Locate every malaria parasite.
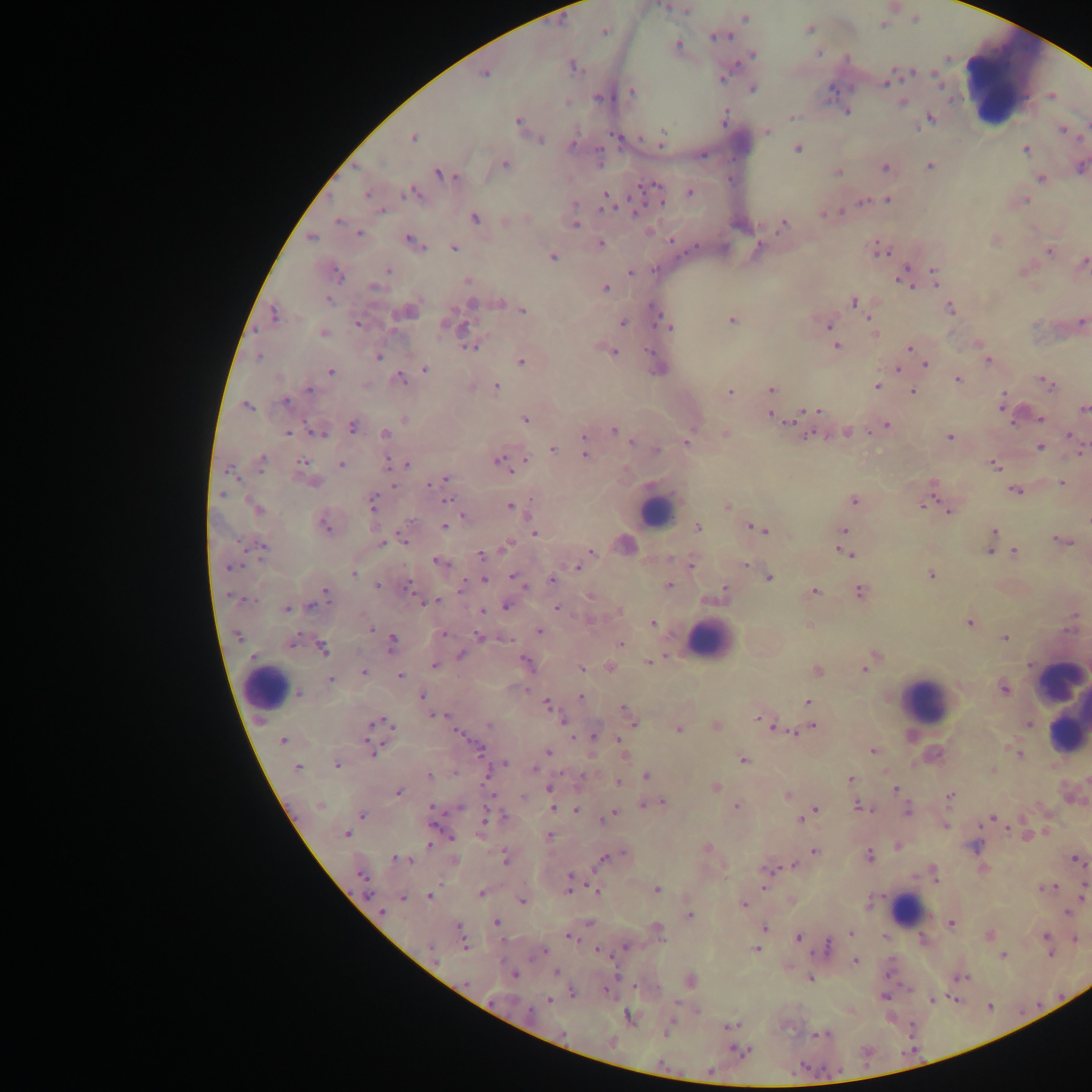

Approximate centers as (x, y) in pixels.
Malaria parasites: (663, 6), (687, 10), (745, 18), (883, 25), (809, 28), (605, 31), (719, 36), (678, 45), (818, 53), (752, 55), (573, 66), (483, 75), (724, 77), (885, 82), (753, 89), (632, 92), (599, 98), (566, 102), (902, 102), (847, 112), (791, 116), (724, 117), (931, 118), (518, 121), (1062, 130), (767, 131), (413, 138), (661, 138), (539, 140), (573, 144), (1025, 149), (797, 150), (505, 165), (930, 166), (1081, 167), (885, 168), (838, 172), (442, 174), (1041, 178), (653, 187), (689, 192), (367, 193), (410, 193), (606, 194), (887, 199), (862, 201), (1025, 201), (575, 204), (606, 206), (635, 208), (382, 211), (826, 213), (476, 219), (338, 220), (575, 225), (782, 225), (360, 234), (311, 238), (412, 241), (601, 244), (454, 248), (757, 249), (882, 252), (1050, 252), (552, 257), (1084, 261), (388, 271), (631, 273), (336, 274), (935, 274), (903, 278), (467, 280), (373, 287), (605, 288), (328, 299), (853, 302), (473, 303), (500, 303), (519, 307), (950, 308), (523, 310), (409, 311), (273, 314), (732, 320), (1082, 320), (623, 323), (359, 324), (828, 325), (452, 326), (667, 326), (874, 332), (323, 333), (837, 346), (471, 347), (909, 348), (614, 352), (649, 352), (379, 356), (259, 357), (988, 361), (521, 362), (926, 364), (898, 368), (424, 369), (331, 372), (401, 380), (959, 380), (1047, 383), (877, 386), (496, 387), (308, 389), (771, 389), (912, 391), (729, 392), (286, 402), (1002, 404), (248, 406), (1083, 409), (818, 411), (771, 416), (1040, 418), (525, 419), (404, 420), (788, 421), (886, 425), (353, 427), (615, 431), (288, 432), (317, 432), (847, 432), (385, 433), (725, 433), (1069, 435), (624, 436), (583, 437), (949, 437), (688, 442), (632, 443), (1041, 446), (552, 449), (657, 450), (585, 455), (525, 459), (261, 461), (301, 461), (388, 462), (499, 462), (408, 463), (341, 465), (994, 465), (229, 471), (445, 479), (316, 482), (1062, 483), (393, 484), (433, 484), (1015, 491), (221, 494), (447, 499), (372, 501), (854, 501), (727, 505), (924, 505), (510, 506), (255, 508), (948, 510), (463, 516), (325, 526), (444, 526), (698, 527), (759, 529), (844, 530), (994, 532), (534, 533), (403, 538), (1062, 541), (990, 542), (382, 543), (507, 545), (262, 547), (590, 551), (990, 551), (846, 552), (1015, 552), (482, 556), (438, 561), (690, 564), (744, 565), (576, 567), (230, 568), (353, 573), (931, 575), (769, 577), (516, 578), (484, 580), (551, 580), (669, 585), (378, 586), (407, 587), (860, 591), (724, 592), (815, 592), (326, 594), (590, 596), (249, 600), (437, 602), (310, 606), (507, 606), (286, 608), (557, 608), (482, 611), (619, 611), (1074, 616), (969, 622), (653, 623), (370, 627), (539, 631), (443, 634), (479, 635), (238, 636), (1004, 638), (508, 640), (292, 642), (392, 642), (620, 643), (322, 648), (461, 655), (872, 659), (649, 661), (527, 663), (435, 666), (610, 667), (581, 669), (865, 669), (817, 670), (364, 672), (400, 676), (330, 681), (1004, 689), (299, 693), (421, 696), (580, 697), (808, 702), (548, 706), (628, 715), (436, 716), (560, 719), (760, 719), (633, 720), (378, 722), (387, 724), (1028, 724), (489, 725), (717, 726), (774, 726), (812, 727), (678, 729), (785, 730), (459, 734), (593, 736), (284, 740), (619, 740), (478, 749), (372, 750), (872, 751), (548, 752), (1016, 752), (743, 760), (504, 763), (336, 765), (298, 767), (535, 770), (646, 776), (430, 777), (850, 778), (618, 783), (715, 786), (896, 789), (550, 790), (398, 792), (787, 795), (523, 797), (949, 797), (656, 802), (320, 805), (649, 805), (431, 806), (736, 806), (859, 806), (460, 807), (552, 809), (814, 810), (576, 811), (907, 811), (810, 814), (362, 815), (612, 815), (493, 816), (486, 817), (801, 818), (991, 818), (946, 826), (346, 834), (549, 836), (430, 845), (975, 846), (706, 847), (898, 847), (816, 852), (617, 855), (870, 856), (505, 858), (604, 859), (400, 860), (1074, 860), (794, 866), (768, 870), (361, 874), (570, 880), (1047, 888), (569, 889), (657, 890), (1084, 890), (597, 891), (481, 893), (367, 894), (429, 896), (403, 898), (522, 901), (743, 905), (381, 912), (1067, 912), (689, 915), (496, 922), (952, 924), (764, 928), (659, 932), (851, 933), (989, 934), (461, 935), (1046, 936), (571, 937), (798, 937), (1076, 939), (465, 943), (625, 947), (826, 947), (756, 950), (432, 951), (542, 952), (1050, 953), (1003, 955), (854, 961), (556, 973), (514, 974), (961, 978), (810, 979), (690, 980), (573, 993), (883, 996), (933, 999), (549, 1001), (630, 1017), (731, 1025), (668, 1028), (820, 1035), (742, 1051), (710, 1071).

{
  "preparation": "thick blood smear",
  "leukocyte_locations": "approximate centers as (x, y) in pixels: (1009, 81), (654, 511), (711, 640), (266, 689), (1060, 696), (927, 700), (1067, 721), (908, 909)",
  "image_size": "1092×1092 pixels",
  "field_of_view": "single",
  "capture": "mobile-phone photograph through a microscope",
  "country": "Ghana"
}